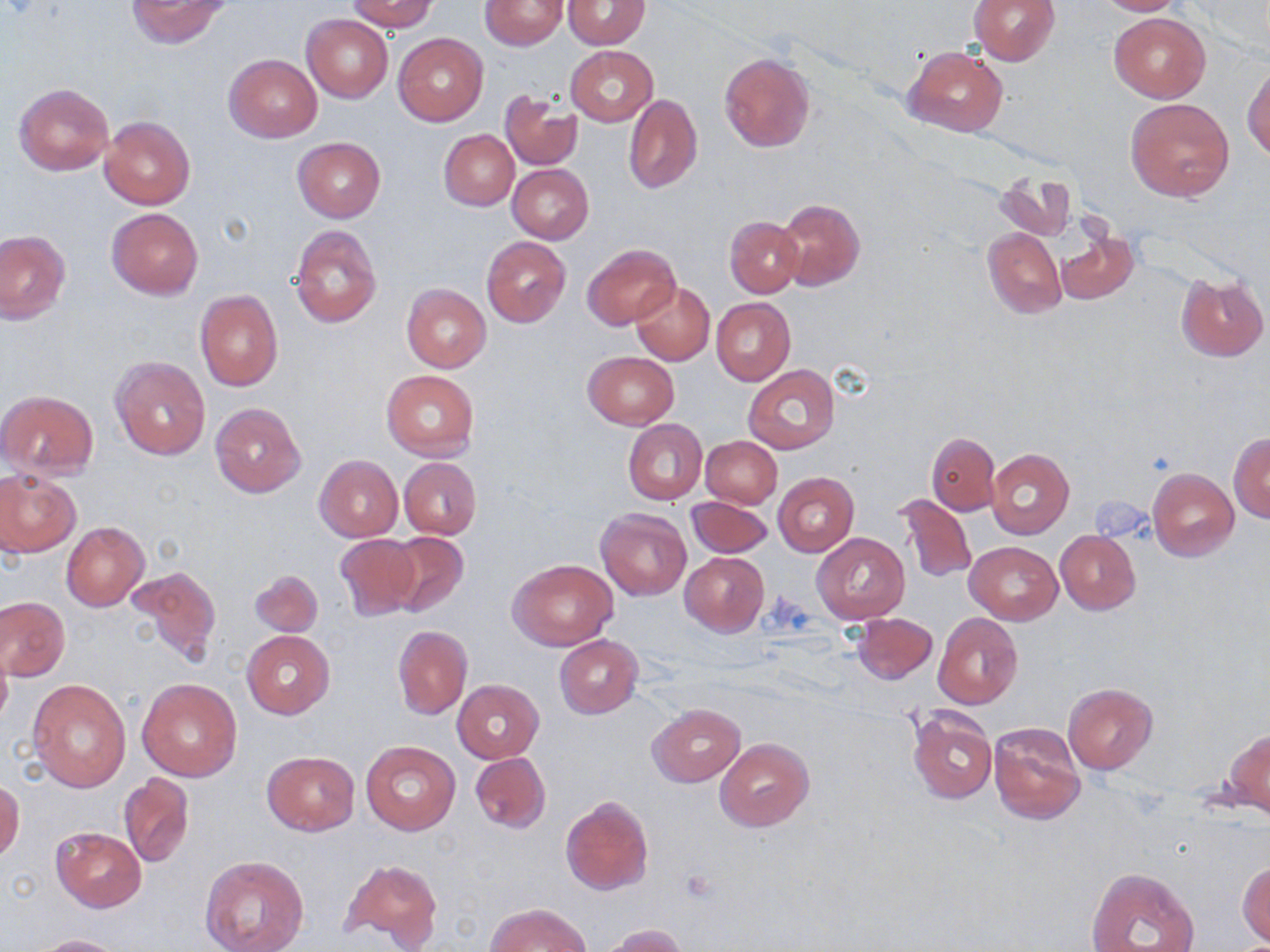
Approximate bounding boxes as (x1,y1)-(x2,y2) corner pairs in pixels. Platelet locations: (680,871)-(720,905). Uninfected red blood cell locations: (347,0)-(438,32), (969,0)-(1059,64), (1090,0)-(1186,16), (126,1)-(232,49), (479,1)-(568,51), (562,1)-(651,49), (1109,13)-(1209,102), (301,14)-(393,102), (394,33)-(488,126), (566,46)-(657,125), (904,46)-(1008,136), (719,52)-(815,153), (224,54)-(321,142), (1243,63)-(1270,162), (14,83)-(113,176), (501,92)-(581,171), (623,94)-(701,195), (1125,97)-(1235,201), (99,115)-(195,210), (439,130)-(519,210), (293,137)-(385,221), (507,164)-(594,243), (995,169)-(1075,243), (775,198)-(864,290), (106,208)-(203,299), (725,216)-(803,297), (290,225)-(382,328), (1055,227)-(1139,308), (982,229)-(1066,318), (0,231)-(71,323), (481,236)-(571,327), (581,244)-(680,330), (1176,273)-(1268,360), (630,280)-(715,366), (402,284)-(491,372), (196,290)-(283,391), (710,297)-(795,385), (583,351)-(678,428), (110,356)-(210,459), (744,365)-(839,453), (381,369)-(479,460), (0,389)-(99,479), (210,402)-(306,498), (624,420)-(706,503), (1229,432)-(1269,522), (926,433)-(1000,514), (701,436)-(782,507), (986,448)-(1074,538), (315,455)-(402,540), (399,457)-(481,538), (1148,467)-(1239,561), (0,470)-(80,557), (774,472)-(858,556), (895,494)-(976,583), (688,496)-(773,558), (595,508)-(692,600), (61,522)-(149,611), (1055,530)-(1141,613), (386,531)-(469,616), (812,532)-(909,626), (334,534)-(420,620), (965,541)-(1062,625), (679,551)-(769,636), (509,559)-(618,651), (126,565)-(219,669), (250,570)-(321,637), (0,596)-(69,681), (852,612)-(937,684), (932,612)-(1023,709), (393,625)-(472,719), (243,630)-(334,720), (555,635)-(643,718), (0,642)-(12,730), (27,678)-(131,792), (138,678)-(243,781), (452,679)-(543,762), (1062,682)-(1158,773), (648,703)-(745,787), (905,706)-(998,805), (988,722)-(1084,825), (1227,730)-(1270,817), (715,738)-(813,831), (360,741)-(460,835), (262,751)-(360,834), (471,752)-(550,834), (119,774)-(193,868), (0,780)-(24,863), (561,796)-(653,895), (51,826)-(146,911), (200,855)-(307,952), (340,859)-(443,949), (1238,859)-(1269,946), (1084,866)-(1201,952), (486,903)-(590,952), (601,924)-(689,952), (29,934)-(123,952). Slide-level diagnosis: negative for blood parasites. May-Grünwald-Giemsa stain. Optical microscopy. Captured at 1000x magnification. Single field of view. Thin blood film. Image is 1270×952 pixels.